Assess this cell for malaria.
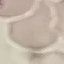
It is uninfected.

Cell patch, automatically extracted from a larger field of view and resized to 64 × 64 pixels. Giemsa stain. Thin blood smear. Acquired by smartphone through the microscope eyepiece.